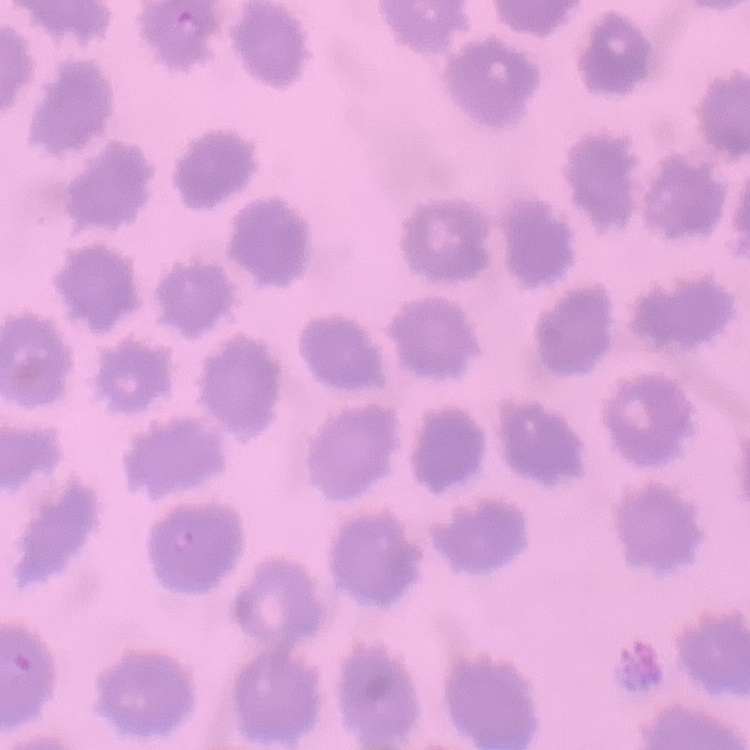

{
  "red_blood_cell_morphology": "no rouleaux formation",
  "stain": "Field's or Giemsa",
  "preparation": "thin blood film",
  "image_type": "one tile cut from a larger photomicrograph"
}